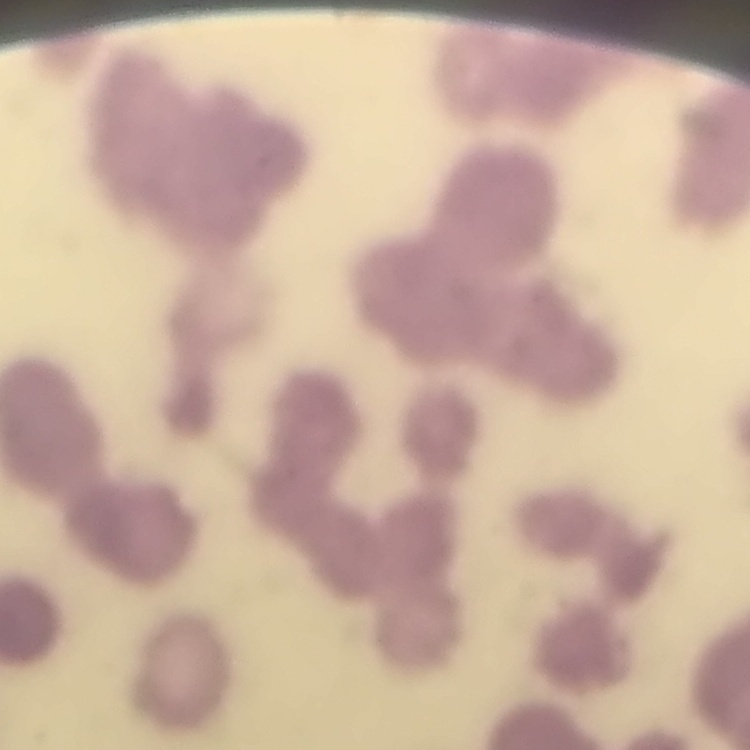
{
  "red_blood_cell_morphology": "rouleaux formation",
  "stain": "Field's or Giemsa",
  "preparation": "thin blood film",
  "image_type": "square crop of a larger photomicrograph"
}